Assess the morphology of the red blood cells.
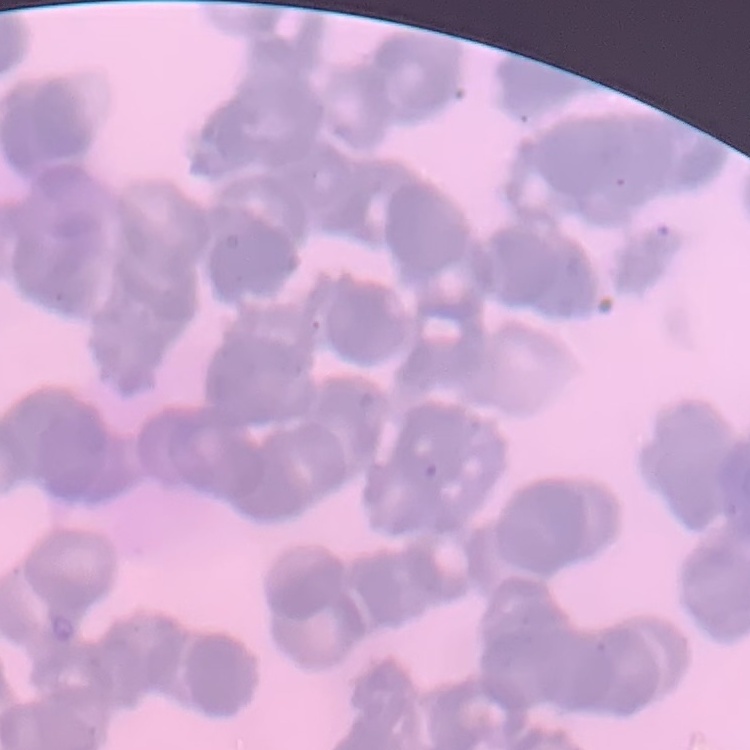

They show rouleaux formation.

Summary:
  - Stain: Field's or Giemsa
  - Preparation: thin blood film
  - Image type: one tile cut from a larger photomicrograph